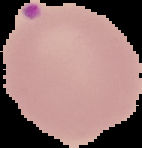
Image is 142×148 pixels. Result: Plasmodium parasites detected. From a thin blood smear. Segmented cell region on a black background.